Point out each malaria parasite.
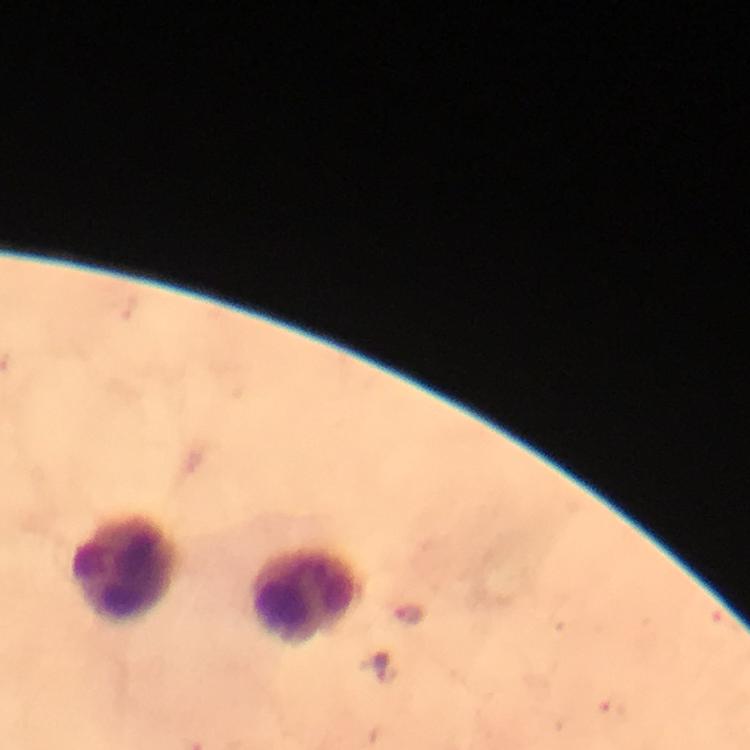

Approximate centers as [x, y] in pixels.
Malaria parasites: [408, 615], [381, 670].

Leukocyte locations: [123, 568], [304, 599]. Cropped region of a single field of view. Immersion oil was used. Giemsa-stained preparation. Photographed with a smartphone mounted on the microscope. From a diagnostic examination for malaria. Image is 750×750 pixels. Thick smear. At 100x magnification.